Name the blood parasite species.
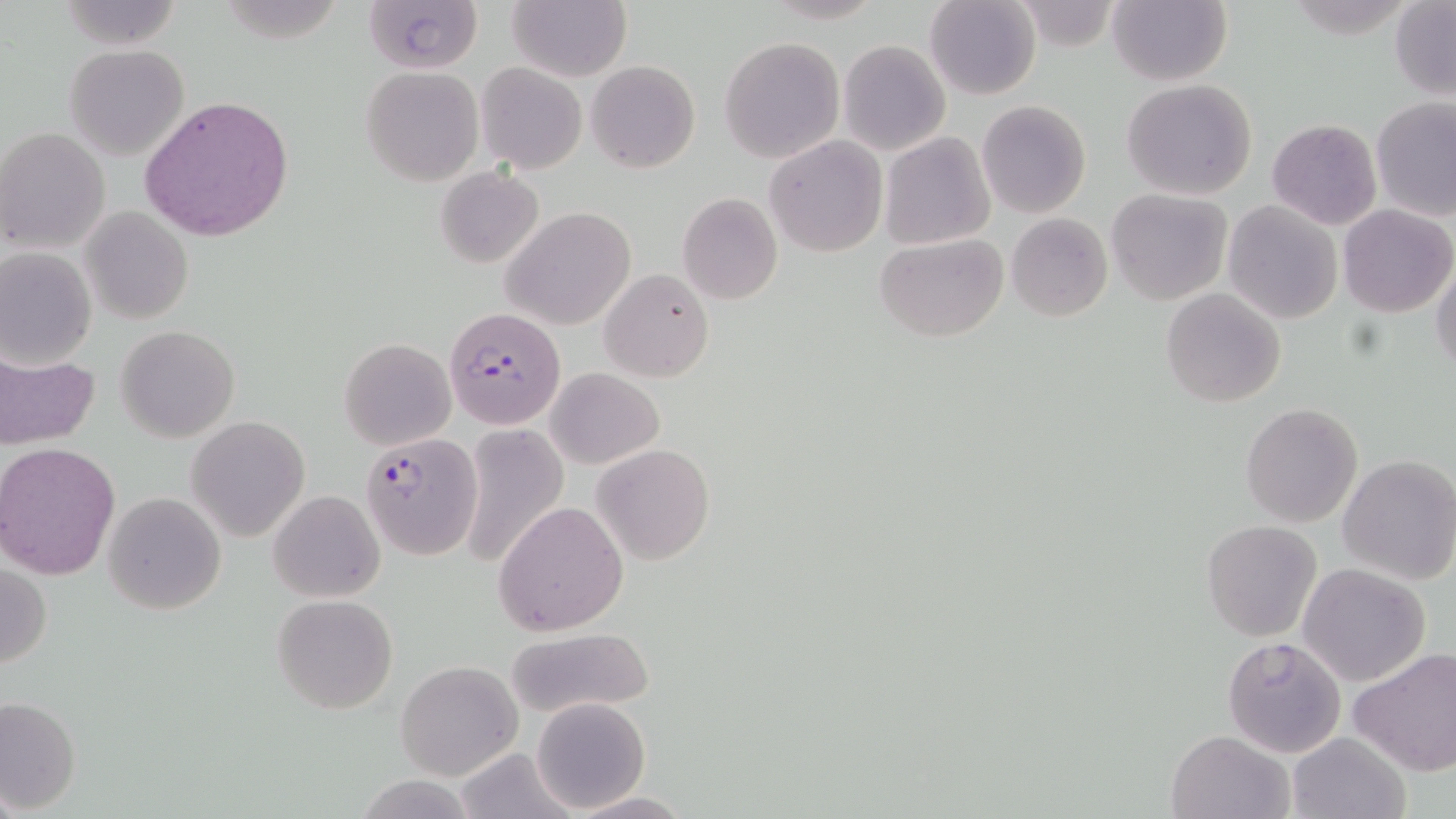
Plasmodium falciparum.

Approximate bounding boxes as named x1/y1/x2/y2 corners in pixels. Uninfected red blood cell locations: (x1=57, y1=0, x2=186, y2=50), (x1=363, y1=0, x2=482, y2=73), (x1=506, y1=0, x2=631, y2=82), (x1=925, y1=0, x2=1041, y2=101), (x1=1107, y1=1, x2=1231, y2=86), (x1=1390, y1=2, x2=1456, y2=100), (x1=719, y1=37, x2=845, y2=163), (x1=838, y1=40, x2=951, y2=156), (x1=64, y1=44, x2=189, y2=161), (x1=476, y1=61, x2=586, y2=172), (x1=587, y1=61, x2=700, y2=173), (x1=361, y1=65, x2=484, y2=186), (x1=1120, y1=79, x2=1259, y2=200), (x1=139, y1=95, x2=295, y2=241), (x1=1373, y1=99, x2=1456, y2=221), (x1=977, y1=100, x2=1090, y2=218), (x1=1266, y1=118, x2=1382, y2=230), (x1=1, y1=129, x2=110, y2=252), (x1=880, y1=131, x2=996, y2=250), (x1=765, y1=136, x2=887, y2=257), (x1=435, y1=166, x2=546, y2=269), (x1=1106, y1=189, x2=1233, y2=307), (x1=677, y1=192, x2=783, y2=304), (x1=1222, y1=201, x2=1343, y2=324), (x1=1338, y1=204, x2=1453, y2=317), (x1=81, y1=205, x2=193, y2=325), (x1=502, y1=207, x2=636, y2=329), (x1=1007, y1=213, x2=1112, y2=322), (x1=875, y1=233, x2=1007, y2=341), (x1=0, y1=248, x2=96, y2=368), (x1=1431, y1=260, x2=1456, y2=376), (x1=599, y1=267, x2=714, y2=383), (x1=1161, y1=287, x2=1286, y2=408), (x1=117, y1=326, x2=239, y2=442), (x1=339, y1=338, x2=456, y2=450), (x1=1, y1=348, x2=100, y2=452), (x1=547, y1=367, x2=664, y2=469), (x1=1241, y1=402, x2=1364, y2=528), (x1=186, y1=417, x2=310, y2=541), (x1=458, y1=423, x2=569, y2=570), (x1=1, y1=443, x2=120, y2=580), (x1=591, y1=443, x2=716, y2=565), (x1=1338, y1=454, x2=1456, y2=584), (x1=268, y1=490, x2=384, y2=603), (x1=102, y1=492, x2=226, y2=614), (x1=495, y1=500, x2=628, y2=634), (x1=1200, y1=520, x2=1322, y2=640), (x1=1, y1=562, x2=52, y2=669), (x1=1299, y1=563, x2=1432, y2=685), (x1=272, y1=594, x2=399, y2=714), (x1=503, y1=626, x2=654, y2=719), (x1=1220, y1=635, x2=1347, y2=757), (x1=1347, y1=646, x2=1456, y2=777), (x1=394, y1=659, x2=523, y2=781), (x1=0, y1=697, x2=81, y2=813), (x1=530, y1=697, x2=650, y2=814), (x1=1168, y1=730, x2=1294, y2=819), (x1=1286, y1=731, x2=1412, y2=819), (x1=453, y1=745, x2=580, y2=819), (x1=565, y1=791, x2=693, y2=818). Plasmodium falciparum-infected red blood cell locations: (x1=444, y1=306, x2=565, y2=430), (x1=362, y1=433, x2=482, y2=558). Thin blood film. Captured at 1000x magnification. May-Grünwald-Giemsa stain. Light microscopy. Image is 1456×819 pixels. One field of a larger specimen.